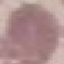

Summary:
  - Malaria status: uninfected
  - Preparation: thin smear
  - Image type: cell patch, automatically extracted from a larger field of view and resized to 64 × 64 pixels
  - Capture: smartphone through the microscope eyepiece
  - Stain: Giemsa